Name the cell type shown.
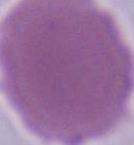
An erythrocyte.

Summary:
  - Magnification: 1000x
  - Modality: photomicrograph